Classify this cell by malaria status.
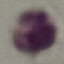
It is uninfected.

Giemsa-stained preparation. Thin blood film. Photographed with a smartphone camera at the microscope eyepiece. Automatically extracted cell patch, resized to 64 × 64 pixels.